State the blood parasite species.
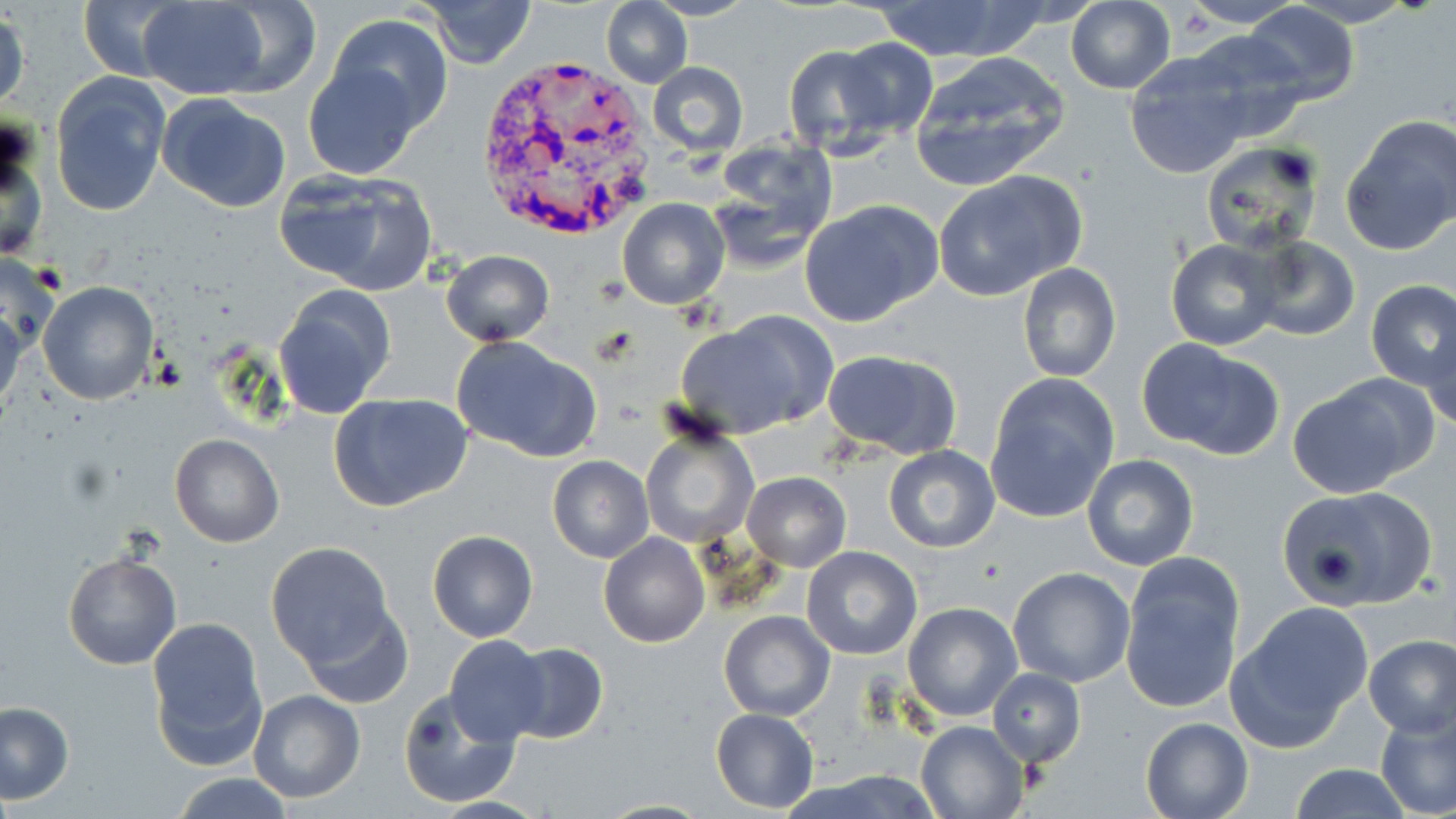
Plasmodium vivax.

modality = optical microscopy
field of view = one of a larger specimen
image size = 1456×819 pixels
preparation = thin blood smear
stain = May-Grünwald-Giemsa
uninfected red blood cell locations = approximate bounding boxes as (x1,y1)-(x2,y2) corner pairs in pixels: (78,0)-(184,81), (419,0)-(537,68), (602,0)-(692,88), (646,0)-(754,21), (873,0)-(1025,62), (1180,0)-(1301,27), (135,1)-(271,99), (204,1)-(323,96), (1065,1)-(1177,94), (1244,2)-(1360,103), (1,5)-(29,116), (329,14)-(453,130), (1183,26)-(1310,142), (837,37)-(938,139), (783,45)-(894,157), (909,51)-(1071,187), (1124,54)-(1251,180), (647,61)-(749,156), (303,62)-(426,180), (49,71)-(172,217), (157,93)-(292,213), (1341,114)-(1455,254), (0,128)-(47,263), (709,136)-(840,257), (1200,142)-(1324,255), (933,170)-(1086,302), (278,171)-(439,296), (617,197)-(731,310), (799,199)-(942,328), (1246,237)-(1360,341), (1166,239)-(1283,350), (440,250)-(554,346), (1017,264)-(1121,382), (1366,280)-(1456,389), (38,281)-(157,404), (273,285)-(397,418), (0,304)-(26,419), (675,311)-(838,439), (1422,322)-(1456,432), (452,336)-(600,460), (1137,339)-(1285,460), (821,349)-(962,458), (984,374)-(1120,524), (1287,375)-(1435,494), (329,392)-(474,513), (640,424)-(759,550), (169,433)-(284,548), (882,445)-(1001,552), (1082,455)-(1199,570), (547,456)-(654,563), (741,472)-(850,572), (1274,484)-(1438,612), (427,530)-(538,642), (597,532)-(710,647), (266,543)-(397,665), (802,546)-(922,659), (61,548)-(181,671), (1120,560)-(1244,714), (1007,566)-(1136,688), (903,602)-(1022,721), (301,603)-(415,712), (1224,606)-(1372,751), (718,611)-(834,721), (146,621)-(268,769), (444,634)-(550,743), (1362,634)-(1455,738), (503,642)-(608,743), (987,668)-(1086,766), (398,688)-(517,809), (247,689)-(365,802), (0,701)-(73,803), (1373,704)-(1456,816), (711,708)-(819,812), (1139,717)-(1253,819), (914,718)-(1030,818), (1287,764)-(1416,819), (170,773)-(297,818), (425,796)-(553,817), (594,798)-(713,818)
magnification = 1000x
Plasmodium vivax-infected red blood cell locations = approximate bounding boxes as (x1,y1)-(x2,y2) corner pairs in pixels: (472,54)-(659,240)